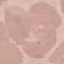
Summary:
  - Malaria status: uninfected
  - Image type: automatically extracted cell patch, resized to 64 × 64 pixels
  - Capture: smartphone camera at the microscope eyepiece
  - Stain: Giemsa
  - Preparation: thin blood smear